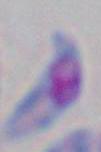
Photomicrograph. 1000x magnification. Toxoplasma gondii is seen.